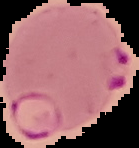

Summary:
  - Image size: 139×148 pixels
  - Result: Plasmodium parasites detected
  - Image type: segmented cell region on a black background
  - Preparation: thin blood film